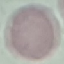
Summary:
  - Result: no malaria parasites seen
  - Preparation: thin smear
  - Image type: automatically extracted cell patch, resized to 64 × 64 pixels
  - Stain: Giemsa
  - Capture: smartphone through the microscope eyepiece